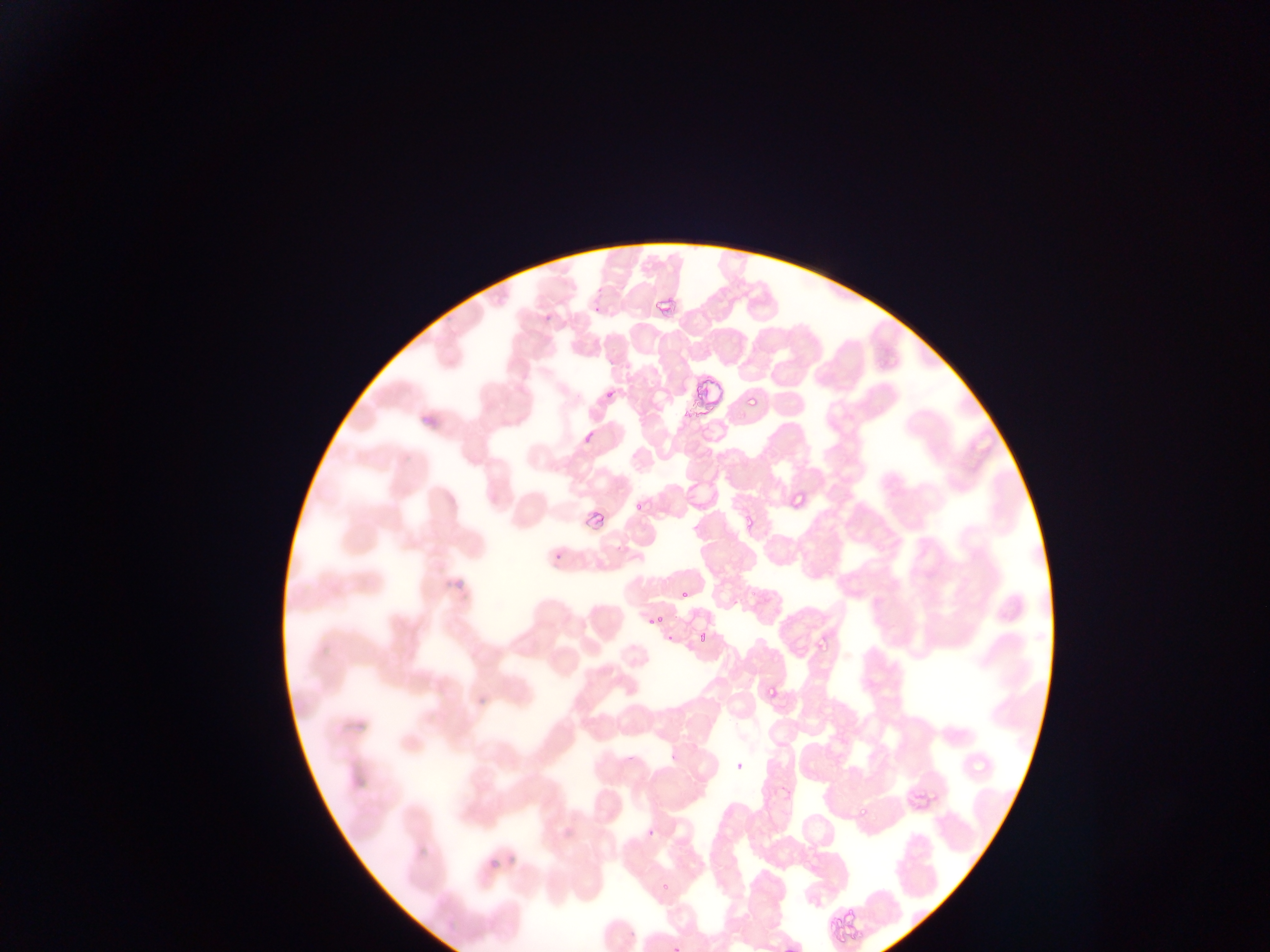
Approximate bounding boxes as [left, top, right, bottom] in pixels.
Summary:
  - Malaria parasite locations: [748, 393, 758, 408], [790, 491, 804, 507], [632, 503, 643, 512], [682, 591, 691, 598], [650, 612, 662, 624], [698, 631, 706, 646], [818, 634, 832, 649], [769, 683, 775, 697], [858, 802, 871, 818], [659, 880, 673, 898]
  - Preparation: thin blood smear
  - Capture: mobile-phone photograph through a microscope
  - Country: Ghana
  - Image size: 1270×952 pixels
  - Field of view: single